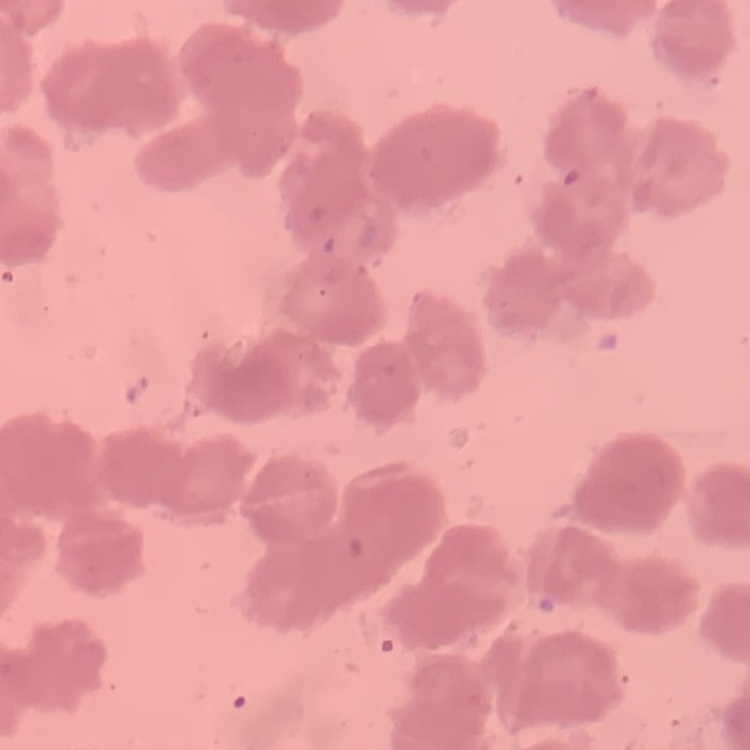
erythrocyte morphology = rouleaux formation
stain = Field's or Giemsa
preparation = thin blood film
image type = square crop of a larger photomicrograph